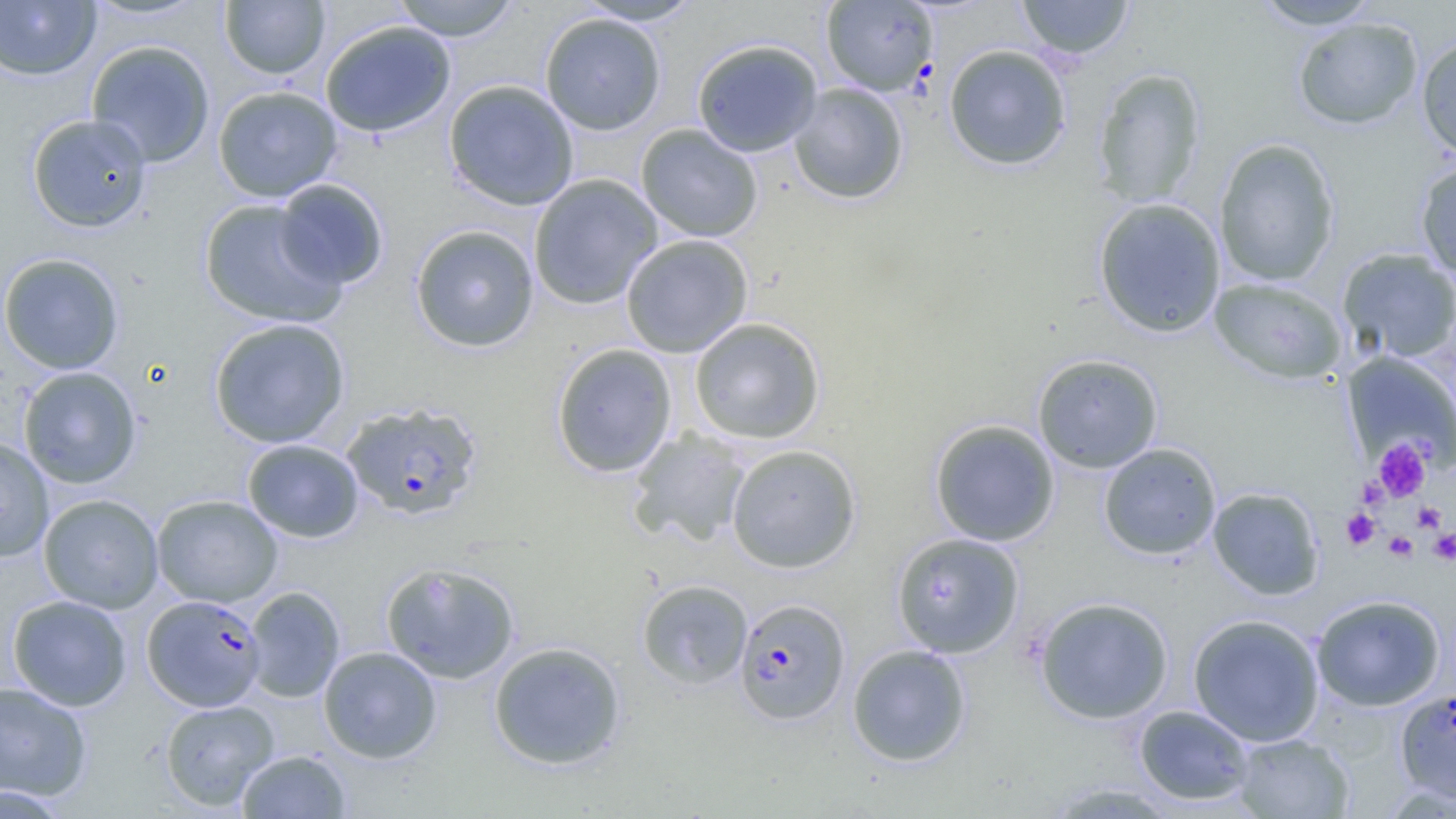
Approximate bounding boxes as named x1/y1/x2/y2 corners in pixels. Uninfected red blood cell locations: (x1=82, y1=0, x2=210, y2=21), (x1=390, y1=0, x2=521, y2=41), (x1=574, y1=0, x2=704, y2=26), (x1=1017, y1=0, x2=1134, y2=60), (x1=1252, y1=0, x2=1382, y2=30), (x1=0, y1=1, x2=100, y2=81), (x1=220, y1=1, x2=330, y2=79), (x1=540, y1=13, x2=667, y2=135), (x1=1292, y1=17, x2=1424, y2=130), (x1=320, y1=20, x2=456, y2=138), (x1=1416, y1=35, x2=1456, y2=160), (x1=691, y1=39, x2=823, y2=157), (x1=85, y1=40, x2=215, y2=168), (x1=943, y1=44, x2=1072, y2=171), (x1=1091, y1=67, x2=1208, y2=209), (x1=443, y1=80, x2=579, y2=211), (x1=789, y1=83, x2=908, y2=205), (x1=212, y1=85, x2=342, y2=202), (x1=27, y1=113, x2=152, y2=233), (x1=636, y1=123, x2=763, y2=242), (x1=1213, y1=138, x2=1341, y2=286), (x1=1415, y1=160, x2=1456, y2=282), (x1=528, y1=174, x2=662, y2=310), (x1=274, y1=178, x2=389, y2=289), (x1=1093, y1=197, x2=1227, y2=338), (x1=199, y1=199, x2=346, y2=328), (x1=410, y1=224, x2=540, y2=353), (x1=621, y1=234, x2=754, y2=358), (x1=1336, y1=248, x2=1456, y2=363), (x1=0, y1=253, x2=125, y2=375), (x1=1208, y1=277, x2=1347, y2=384), (x1=689, y1=317, x2=826, y2=444), (x1=209, y1=318, x2=350, y2=448), (x1=551, y1=343, x2=678, y2=477), (x1=1342, y1=352, x2=1456, y2=472), (x1=1032, y1=353, x2=1164, y2=473), (x1=17, y1=366, x2=142, y2=489), (x1=929, y1=419, x2=1060, y2=546), (x1=628, y1=429, x2=753, y2=547), (x1=0, y1=436, x2=54, y2=562), (x1=242, y1=438, x2=364, y2=543), (x1=1098, y1=442, x2=1222, y2=560), (x1=726, y1=444, x2=862, y2=573), (x1=1207, y1=486, x2=1325, y2=600), (x1=38, y1=493, x2=163, y2=614), (x1=151, y1=494, x2=283, y2=608), (x1=891, y1=532, x2=1024, y2=658), (x1=380, y1=561, x2=520, y2=685), (x1=636, y1=579, x2=753, y2=690), (x1=244, y1=587, x2=345, y2=702), (x1=8, y1=594, x2=132, y2=711), (x1=1311, y1=594, x2=1446, y2=711), (x1=1033, y1=596, x2=1174, y2=723), (x1=1187, y1=613, x2=1325, y2=747), (x1=488, y1=641, x2=627, y2=770), (x1=847, y1=644, x2=971, y2=766), (x1=318, y1=646, x2=442, y2=763), (x1=0, y1=682, x2=92, y2=802), (x1=160, y1=699, x2=279, y2=811), (x1=1133, y1=705, x2=1255, y2=806), (x1=1233, y1=733, x2=1354, y2=818), (x1=237, y1=750, x2=351, y2=818), (x1=1043, y1=782, x2=1183, y2=818), (x1=0, y1=784, x2=72, y2=818). Plasmodium falciparum-infected red blood cell locations: (x1=822, y1=1, x2=938, y2=95), (x1=341, y1=401, x2=483, y2=521), (x1=142, y1=594, x2=266, y2=711), (x1=734, y1=597, x2=851, y2=726), (x1=1396, y1=688, x2=1456, y2=804). Platelet locations: (x1=1373, y1=438, x2=1431, y2=502), (x1=1356, y1=476, x2=1389, y2=509), (x1=1412, y1=502, x2=1446, y2=532), (x1=1341, y1=508, x2=1380, y2=550), (x1=1428, y1=528, x2=1456, y2=565), (x1=1383, y1=531, x2=1418, y2=562). Slide-level diagnosis: Plasmodium falciparum. One field of a larger specimen. Image is 1456×819 pixels. Light microscopy. Thin blood smear. Captured at 1000x magnification.